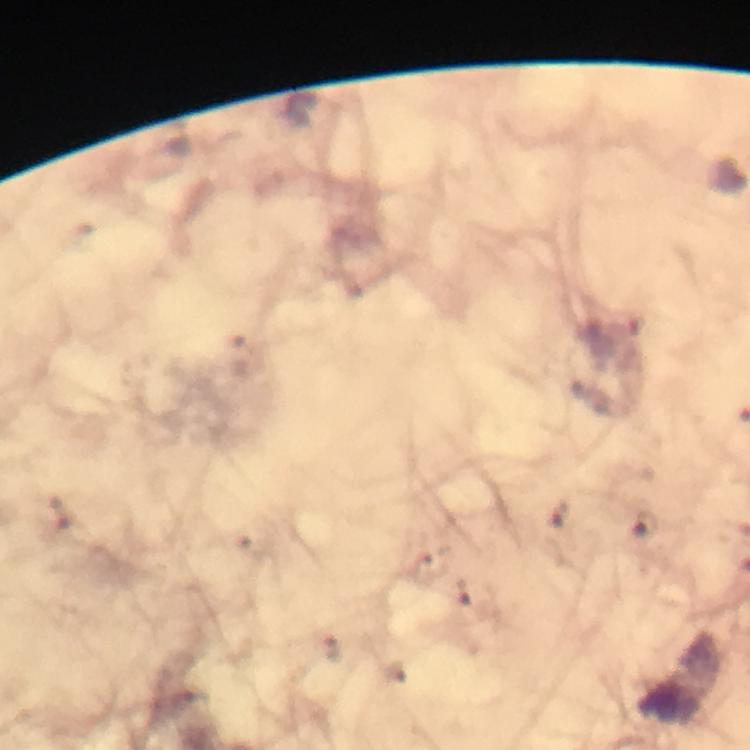
{
  "stain": "Giemsa",
  "immersion_oil": "used",
  "malaria_parasite_locations": "approximate object centers, in pixels from the top-left corner (list possibly incomplete): (x=645, y=525)",
  "context": "from a diagnostic examination for malaria",
  "magnification": "100x",
  "preparation": "thick blood smear",
  "image_size": "750×750 pixels",
  "cropped_from": "a single field of view",
  "capture": "smartphone mounted on the microscope"
}